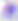

Toxoplasma gondii is seen. Micrograph. Captured at 400x magnification.